Locate and identify every blood parasite.
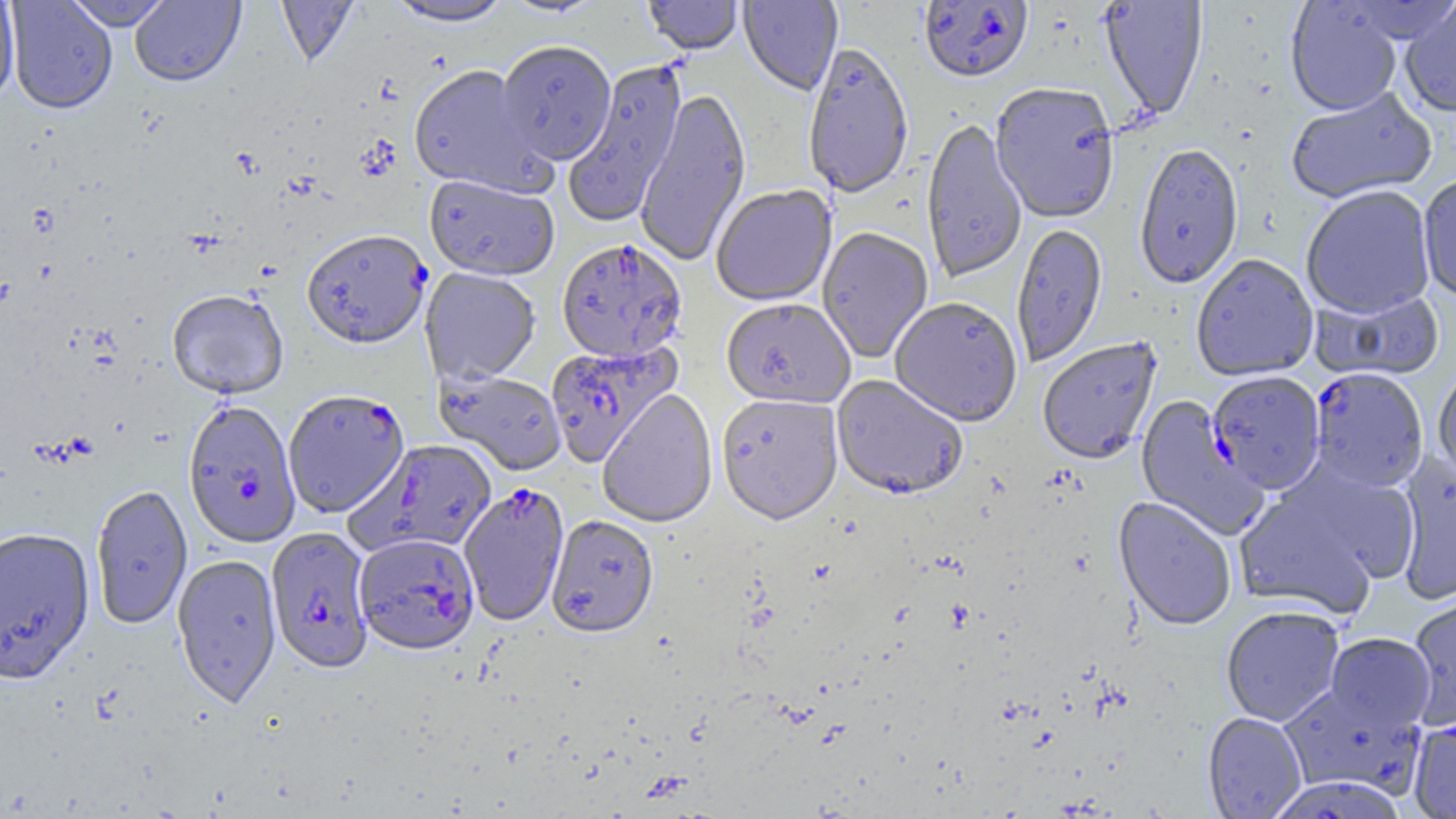

Approximate bounding boxes as (x1, y1, x2, y2) in pixels.
Plasmodium falciparum-infected red blood cells (subset): (919, 1, 1034, 86), (557, 239, 687, 362), (546, 341, 682, 467), (1309, 369, 1428, 493), (1208, 371, 1325, 496), (283, 390, 410, 518), (190, 401, 308, 548), (347, 439, 498, 557), (265, 527, 375, 673), (352, 533, 480, 655), (1268, 776, 1406, 818).
No Plasmodium ovale, Plasmodium malariae, Plasmodium vivax, Babesia divergens, or Trypanosoma brucei observed.

slide-level diagnosis = Plasmodium falciparum
preparation = thin blood smear
field of view = single
magnification = 1000x
modality = light microscopy
uninfected red blood cell locations (subset) = approximate bounding boxes as (x1, y1, x2, y2) in pixels: (5, 0, 117, 115), (130, 0, 245, 88), (275, 0, 360, 68), (499, 0, 606, 19), (642, 0, 744, 56), (738, 0, 843, 96), (1100, 0, 1209, 121), (0, 1, 20, 105), (62, 1, 175, 31), (384, 1, 514, 28), (1285, 2, 1402, 117), (1398, 2, 1456, 119), (496, 42, 616, 166), (802, 43, 915, 201), (563, 59, 688, 228), (408, 65, 551, 196), (990, 84, 1120, 225), (634, 88, 751, 269), (1286, 89, 1437, 205), (921, 119, 1028, 284), (1134, 145, 1244, 290), (424, 175, 560, 282), (1417, 175, 1456, 304), (711, 186, 836, 307), (1301, 186, 1436, 321), (1011, 224, 1109, 369), (817, 228, 933, 364), (1191, 255, 1320, 382), (420, 268, 541, 385), (1313, 287, 1445, 383), (167, 290, 289, 400), (721, 298, 855, 410), (890, 298, 1023, 428), (1037, 338, 1162, 465), (1433, 366, 1456, 487), (435, 369, 567, 476), (832, 376, 968, 501), (598, 389, 718, 529), (716, 394, 844, 527), (1135, 396, 1269, 541), (1395, 452, 1456, 607), (1232, 470, 1405, 618), (90, 483, 193, 630), (1113, 497, 1237, 632), (547, 515, 658, 640), (0, 527, 95, 684), (172, 553, 282, 707), (1406, 587, 1456, 732), (1221, 607, 1344, 726), (1324, 633, 1435, 733), (1279, 683, 1426, 799), (1202, 712, 1307, 819), (1408, 719, 1456, 818)
image size = 1456×819 pixels